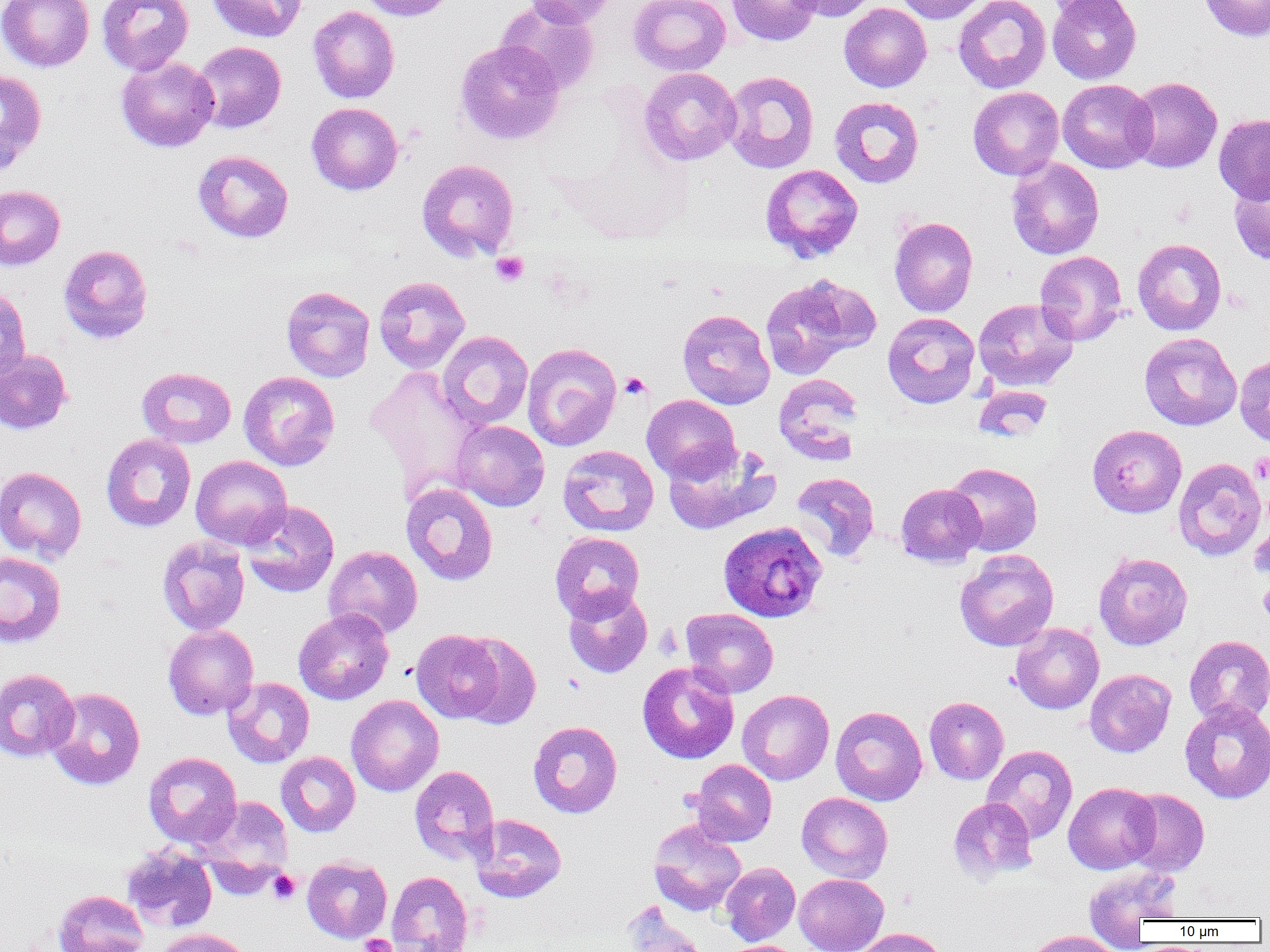

{
  "slide_level_diagnosis": "Plasmodium ovale",
  "uninfected_red_blood_cell_locations": "approximate bounding boxes as (x1,y1)-(x2,y2) corner pairs in pixels: (0,0)-(94,72), (96,0)-(195,75), (208,0)-(307,42), (357,0)-(458,21), (525,0)-(616,28), (629,0)-(730,76), (727,0)-(821,46), (787,0)-(880,21), (893,0)-(990,24), (953,0)-(1051,93), (1042,0)-(1134,19), (1047,0)-(1141,84), (1199,0)-(1270,41), (496,2)-(599,94), (839,3)-(932,92), (308,6)-(399,103), (455,39)-(565,145), (192,41)-(286,134), (116,56)-(219,152), (639,67)-(741,165), (0,69)-(47,173), (722,70)-(820,174), (1127,76)-(1222,173), (1057,79)-(1157,173), (967,86)-(1064,181), (829,96)-(925,188), (306,103)-(403,195), (1213,113)-(1270,205), (193,149)-(294,243), (1006,157)-(1104,260), (417,159)-(519,262), (760,164)-(863,262), (1228,177)-(1270,264), (0,185)-(65,271), (889,217)-(978,317), (1132,238)-(1226,335), (58,244)-(153,343), (1034,251)-(1127,346), (798,275)-(881,355), (373,276)-(470,373), (761,279)-(855,380), (0,286)-(31,383), (281,286)-(375,382), (973,298)-(1078,391), (677,309)-(775,409), (882,312)-(980,409), (437,331)-(533,429), (1139,332)-(1242,430), (522,342)-(621,451), (0,348)-(73,435), (1234,354)-(1270,447), (365,365)-(485,497), (137,367)-(236,448), (238,371)-(340,470), (773,374)-(864,465), (972,384)-(1053,442), (642,395)-(741,483), (451,420)-(549,511), (1087,425)-(1187,518), (100,433)-(196,532), (662,442)-(779,535), (557,445)-(659,537), (191,455)-(292,550), (1173,458)-(1267,561), (945,462)-(1042,556), (0,466)-(87,563), (791,472)-(879,562), (401,483)-(498,585), (896,483)-(985,567), (240,500)-(340,598), (1249,508)-(1270,586), (550,532)-(645,622), (156,536)-(250,635), (323,546)-(423,639), (955,549)-(1059,651), (0,551)-(66,649), (1093,551)-(1193,650), (563,587)-(652,678), (293,608)-(393,705), (680,608)-(779,698), (1010,623)-(1104,714), (163,624)-(259,720), (411,629)-(507,723), (454,633)-(541,729), (1184,635)-(1270,725), (637,662)-(739,763), (0,668)-(79,762), (1084,669)-(1176,757), (223,677)-(315,768), (45,687)-(146,790), (737,689)-(834,785), (346,695)-(444,796), (924,696)-(1008,785), (1180,699)-(1270,803), (830,705)-(928,806), (527,721)-(622,818), (982,745)-(1078,843), (143,751)-(242,848), (276,751)-(360,836), (689,759)-(776,846), (409,765)-(500,865), (1063,782)-(1160,874), (1122,788)-(1209,877), (797,792)-(893,883), (198,796)-(293,879), (948,798)-(1038,883), (470,813)-(567,902), (648,820)-(746,916), (121,844)-(217,933), (302,856)-(392,943), (720,862)-(800,945), (1083,866)-(1182,942), (386,870)-(473,951), (794,874)-(888,952), (53,889)-(149,952), (622,903)-(709,952), (854,927)-(948,952), (156,928)-(255,952), (1023,930)-(1122,952)",
  "preparation": "thin blood smear",
  "platelet_locations": "approximate bounding boxes as (x1,y1)-(x2,y2) corner pairs in pixels: (491,252)-(529,287), (619,372)-(651,399), (1250,452)-(1270,484), (1258,581)-(1270,622), (268,870)-(300,904), (360,934)-(395,952)",
  "image_size": "1270×952 pixels",
  "magnification": "1000x",
  "modality": "optical microscopy",
  "plasmodium_ovale_infected_red_blood_cell_locations": "approximate bounding boxes as (x1,y1)-(x2,y2) corner pairs in pixels: (717,519)-(827,622)",
  "field_of_view": "one of a larger specimen"
}